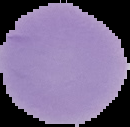

Summary:
  - Result: no Plasmodium parasites detected
  - Preparation: thin blood smear
  - Image size: 130×127 pixels
  - Image type: segmented cell region on a black background